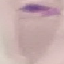

malaria status = uninfected
stain = Giemsa
image type = automatically extracted cell patch, resized to 64 × 64 pixels
capture = smartphone through the microscope eyepiece
preparation = thin blood smear